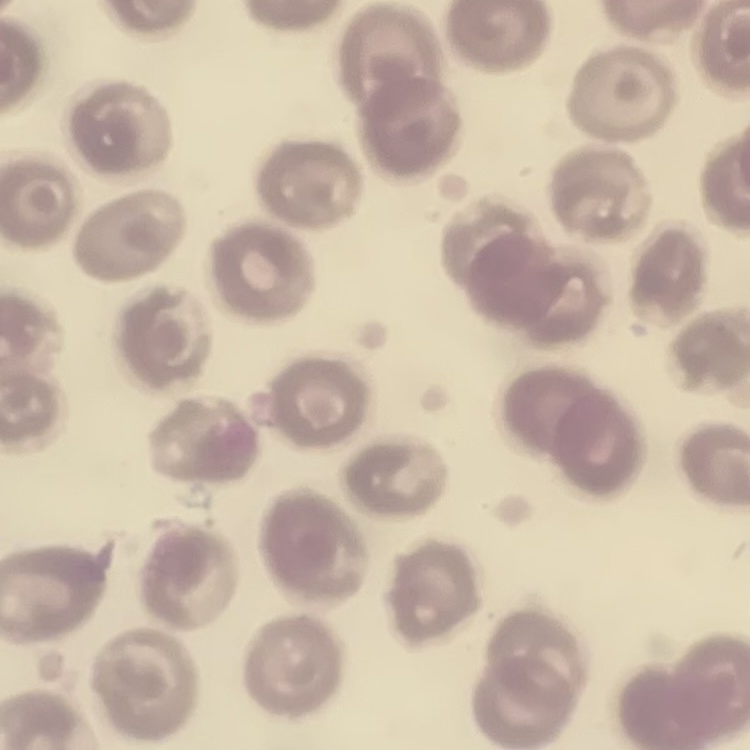
Summary:
  - Red blood cell morphology: no rouleaux formation
  - Image type: square crop of a larger photomicrograph
  - Stain: Field's or Giemsa
  - Preparation: thin blood film